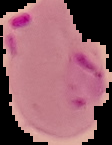

image size = 112×145 pixels
malaria status = parasitized
preparation = thin blood smear
image type = segmented cell region on a black background